Comment on the morphology of the erythrocytes.
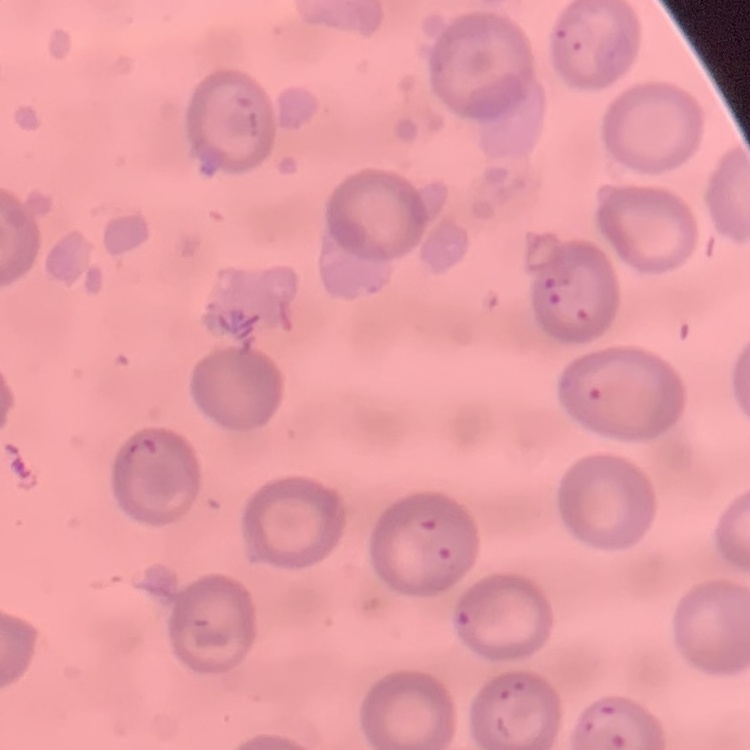

They show no rouleaux formation.

Summary:
  - Stain: Field's or Giemsa
  - Preparation: thin blood smear
  - Image type: square crop of a larger photomicrograph